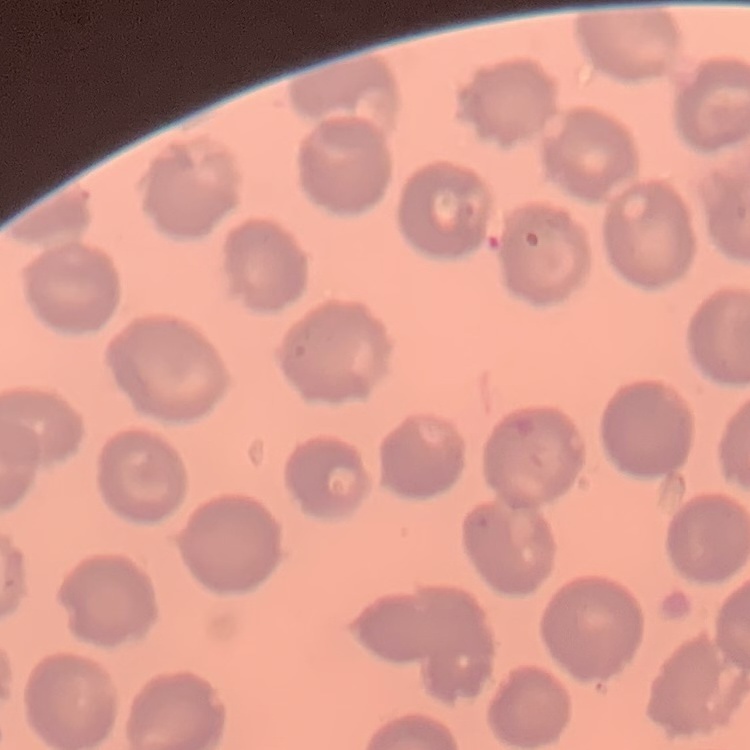

The erythrocytes exhibit no rouleaux formation. Square crop of a larger photomicrograph. Thin blood film. Stained with either Field's or Giemsa.